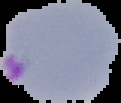

preparation = thin blood film
image type = segmented cell region on a black background
malaria status = parasitized
image size = 121×103 pixels